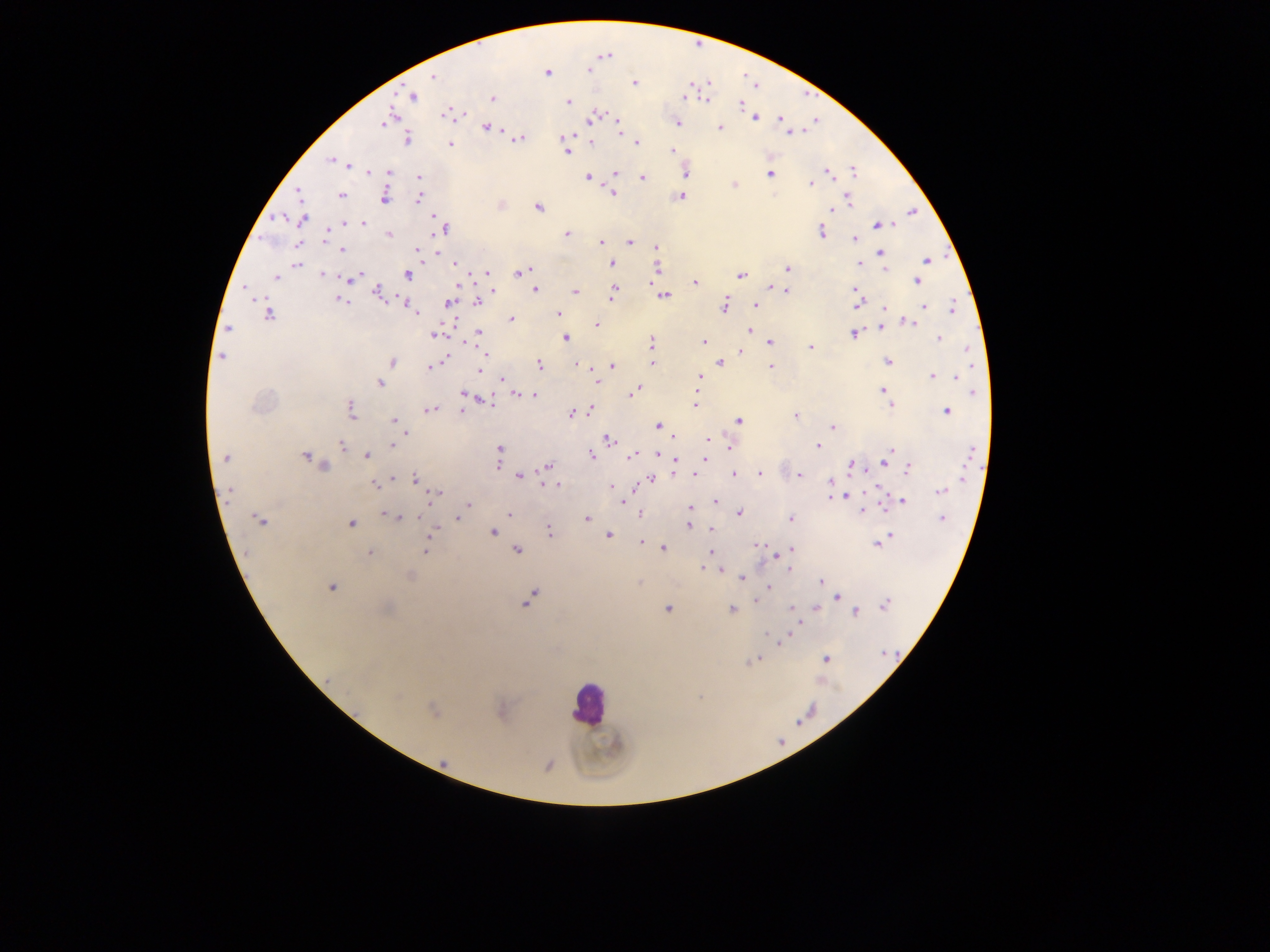
Approximate centers as (x, y) in pixels.
Summary:
  - Malaria parasite locations: (604, 55), (590, 69), (547, 73), (432, 77), (634, 83), (412, 96), (685, 97), (707, 97), (492, 98), (568, 101), (740, 104), (450, 112), (750, 114), (781, 116), (591, 117), (755, 117), (388, 118), (616, 121), (677, 122), (486, 126), (784, 126), (719, 127), (805, 129), (789, 132), (518, 138), (564, 138), (407, 139), (591, 141), (637, 142), (450, 144), (672, 150), (567, 152), (333, 161), (347, 164), (684, 171), (370, 172), (389, 172), (826, 172), (615, 173), (769, 173), (853, 173), (418, 177), (588, 177), (642, 177), (811, 184), (734, 185), (300, 192), (612, 192), (340, 195), (383, 195), (681, 195), (419, 198), (848, 200), (538, 207), (829, 209), (912, 211), (302, 219), (435, 219), (343, 224), (364, 224), (878, 224), (890, 225), (444, 227), (821, 231), (388, 234), (566, 234), (325, 236), (853, 239), (599, 241), (630, 241), (656, 248), (342, 250), (418, 251), (880, 253), (657, 255), (927, 259), (456, 263), (297, 264), (611, 264), (859, 264), (656, 266), (787, 268), (884, 268), (520, 272), (487, 273), (322, 275), (358, 275), (406, 275), (740, 275), (276, 277), (348, 278), (916, 280), (651, 281), (694, 282), (770, 285), (246, 289), (535, 289), (787, 289), (853, 289), (492, 291), (575, 291), (378, 292), (612, 292), (857, 294), (663, 295), (339, 299), (404, 302), (450, 302), (477, 302), (856, 302), (724, 304), (757, 304), (411, 306), (922, 306), (884, 307), (951, 309), (413, 310), (269, 313), (558, 313), (511, 320), (908, 321), (597, 324), (879, 327), (228, 328), (750, 331), (479, 332), (854, 333), (435, 334), (566, 338), (939, 338), (651, 342), (703, 342), (769, 342), (811, 345), (741, 352), (485, 353), (221, 356), (443, 357), (887, 360), (391, 362), (652, 362), (718, 362), (576, 363), (539, 364), (612, 365), (771, 366), (430, 367), (590, 367), (480, 370), (931, 375), (954, 377), (700, 378), (502, 379), (379, 382), (596, 382), (697, 382), (883, 391), (632, 392), (974, 392), (697, 393), (464, 394), (514, 394), (535, 395), (484, 400), (891, 405), (695, 406), (350, 409), (428, 409), (462, 409), (583, 410), (589, 410), (946, 411), (571, 413), (796, 416), (394, 420), (738, 421), (658, 426), (832, 427), (406, 432), (608, 439), (673, 439), (707, 440), (342, 444), (727, 445), (818, 445), (392, 446), (500, 448), (890, 449), (590, 454), (366, 455), (632, 455), (657, 455), (305, 456), (226, 457), (675, 458), (310, 460), (886, 461), (498, 463), (324, 465), (850, 465), (548, 466), (908, 468), (673, 472), (694, 474), (733, 474), (759, 474), (798, 475), (519, 476), (415, 478), (392, 479), (651, 479), (830, 481), (375, 484), (556, 484), (548, 485), (610, 486), (879, 490), (941, 490), (228, 492), (436, 494), (846, 496), (831, 497), (902, 500), (622, 502), (715, 502), (900, 502), (883, 504), (467, 505), (690, 507), (862, 511), (738, 512), (386, 513), (509, 513), (640, 514), (400, 517), (457, 518), (789, 518), (942, 518), (587, 519), (260, 521), (351, 524), (688, 525), (711, 528), (434, 531), (549, 531), (492, 532), (607, 535), (890, 535), (882, 540), (641, 543), (877, 544), (758, 545), (663, 548), (516, 549), (424, 550), (790, 550), (368, 552), (710, 552), (774, 557), (702, 567), (719, 569), (409, 576), (742, 577), (637, 582), (820, 582), (768, 586), (331, 587), (836, 597), (529, 599), (757, 599), (884, 604), (790, 607), (668, 608), (814, 608), (732, 609), (855, 612), (795, 624), (767, 633), (782, 641), (825, 659), (754, 660), (433, 709), (443, 761), (547, 764)
  - Leukocyte locations: (588, 703)
  - Field of view: single
  - Preparation: thick blood film
  - Capture: mobile-phone photograph through a microscope
  - Image size: 1270×952 pixels
  - Country: Ghana